State which parasite is depicted.
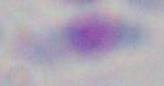
Toxoplasma gondii.

Summary:
  - Modality: micrograph
  - Magnification: 1000x